Locate every Plasmodium parasite.
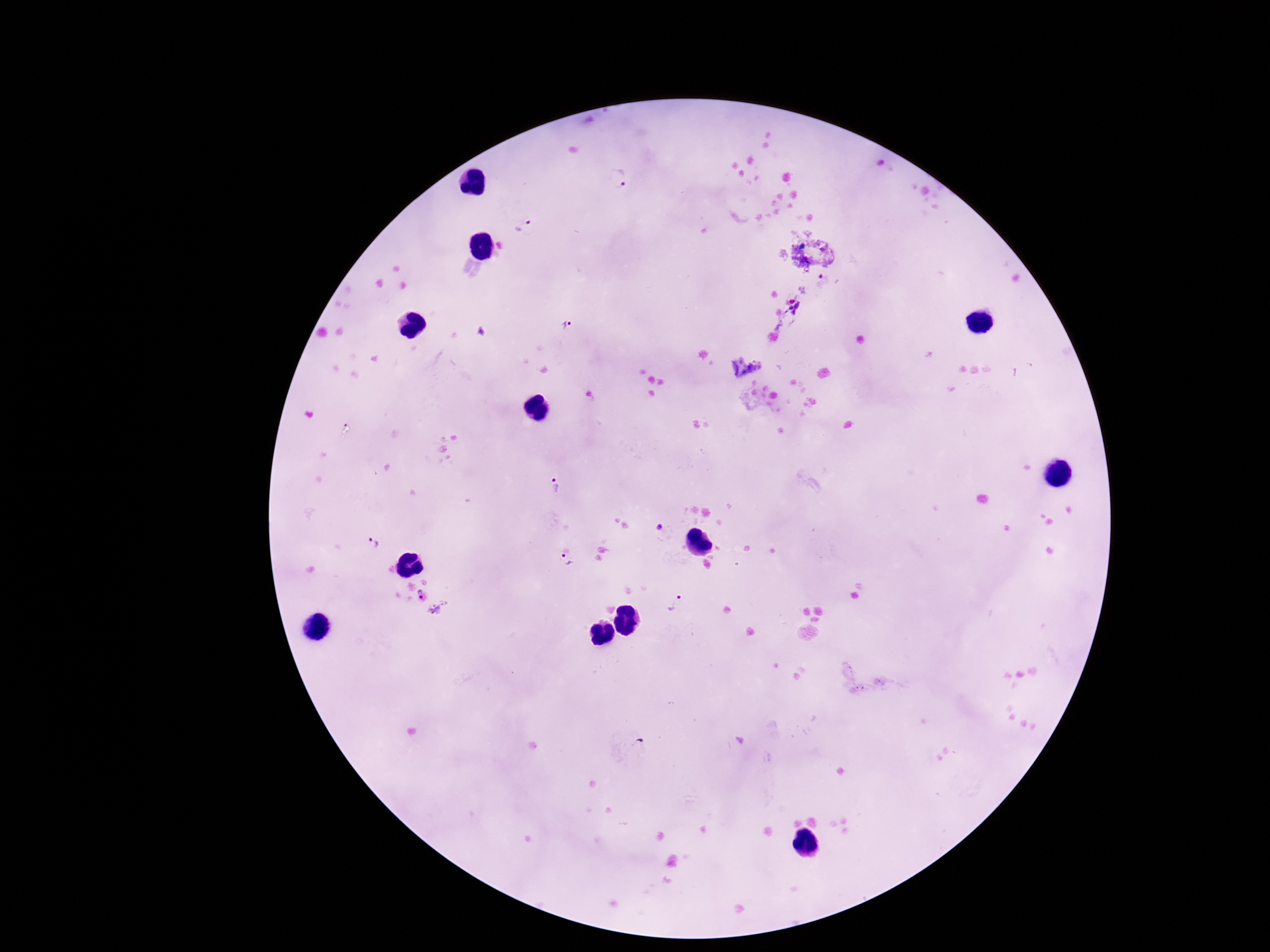

Approximate centers as {x, y} in pixels.
Plasmodium parasites: {618, 179}, {523, 227}, {568, 326}, {555, 488}, {659, 524}, {371, 543}, {564, 560}, {421, 595}, {675, 603}.

Giemsa-stained preparation. Image is 1270×952 pixels. Patient malaria status: infected. Photographed through the microscope eyepiece with a smartphone camera. 100x magnification. One field from this slide. Thick blood film.